Report the malaria status of this cell.
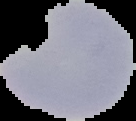

It is uninfected.

Summary:
  - Preparation: thin blood film
  - Image type: segmented cell region on a black background
  - Image size: 136×121 pixels